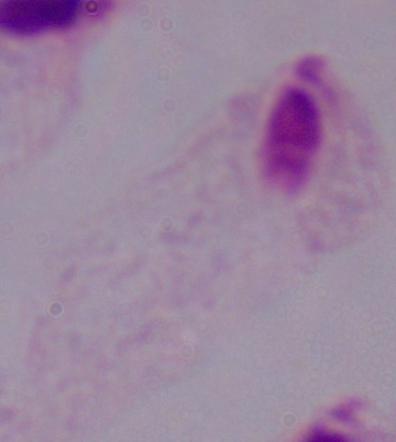
Micrograph. A trichomonad is seen. Captured at 1000x magnification.